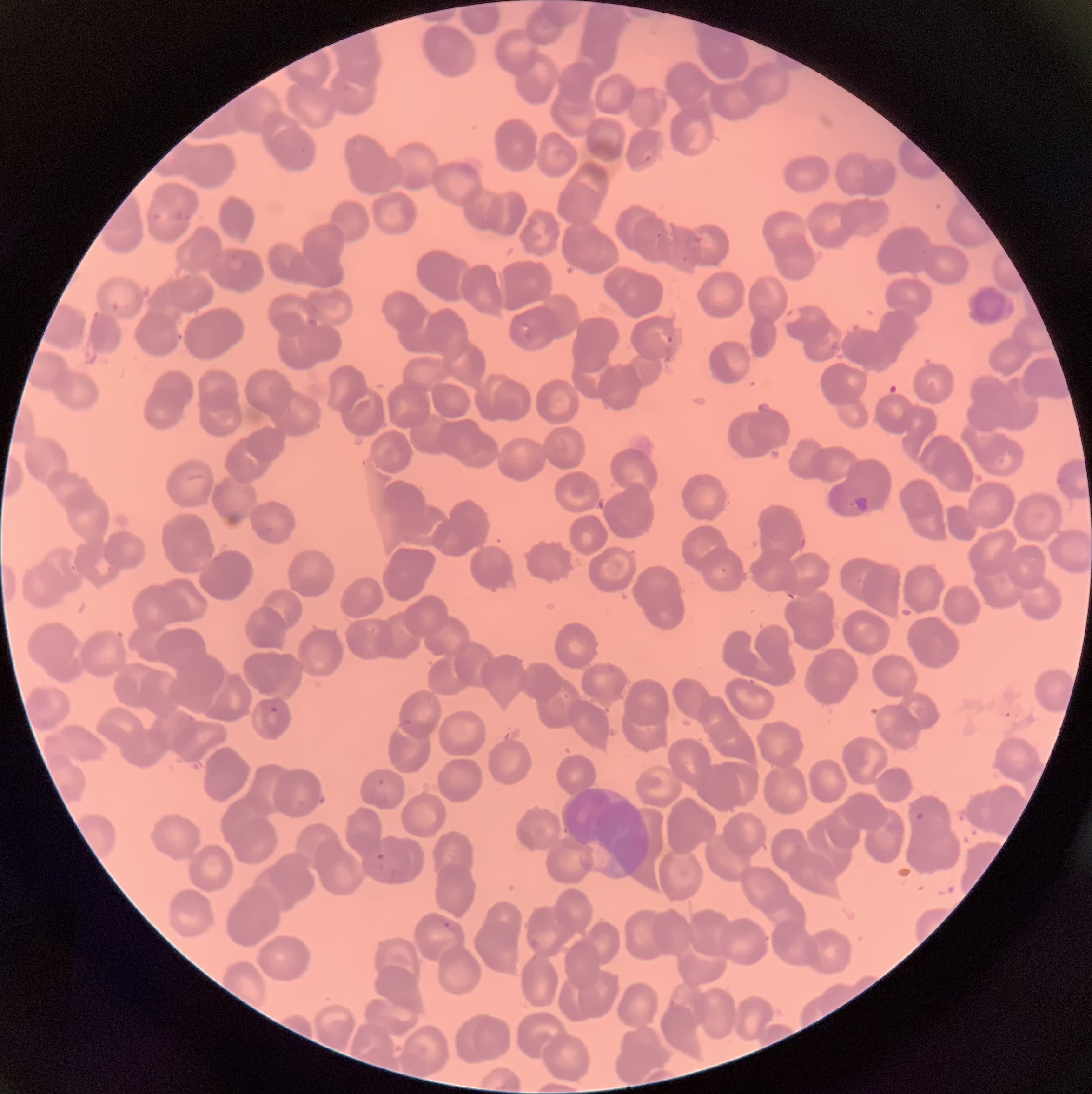 Approximate bounding boxes as named x1/y1/x2/y2 corners in pixels. White blood cell locations: (x1=964, y1=283, x2=1014, y2=328). Plasmodium parasites too small for a box (approximate object centers, named x/y in pixels): (x=659, y=235). Plasmodium parasite locations: (x1=639, y1=149, x2=653, y2=163), (x1=173, y1=211, x2=192, y2=222), (x1=153, y1=213, x2=163, y2=221), (x1=227, y1=253, x2=248, y2=273), (x1=110, y1=300, x2=121, y2=312), (x1=784, y1=306, x2=805, y2=326), (x1=520, y1=321, x2=533, y2=337), (x1=656, y1=331, x2=676, y2=346), (x1=663, y1=354, x2=673, y2=362), (x1=851, y1=494, x2=871, y2=513), (x1=267, y1=705, x2=280, y2=725), (x1=377, y1=778, x2=386, y2=788), (x1=915, y1=812, x2=925, y2=821), (x1=376, y1=852, x2=388, y2=863), (x1=443, y1=921, x2=455, y2=932). The red blood cells show rouleaux formation. Thin blood film. Optical microscopy. Image is 1092×1094 pixels.